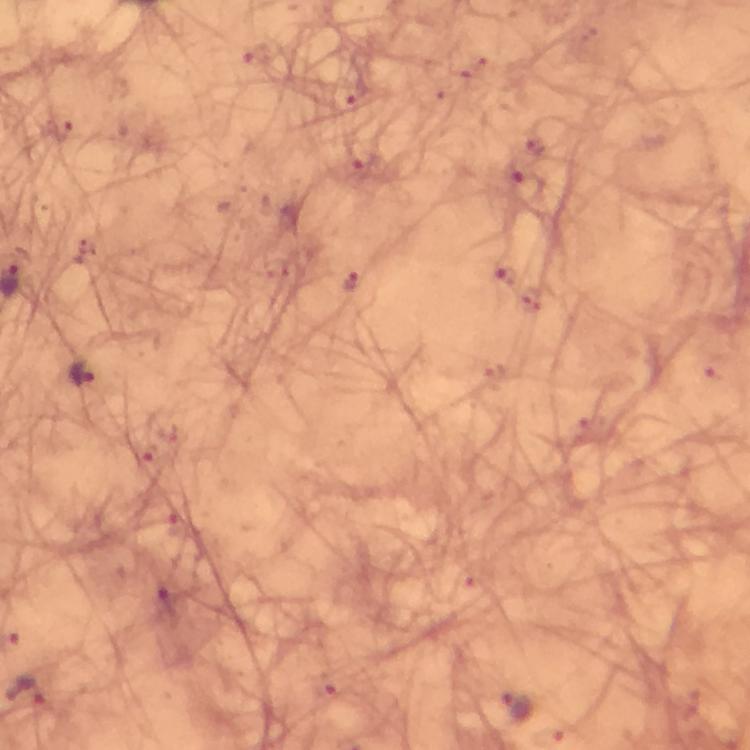 Approximate object centers, in pixels from the top-left corner. Plasmodium parasite locations: (x=350, y=283), (x=83, y=374), (x=27, y=695), (x=514, y=708). Cropped region of a single field of view. From a diagnostic examination for malaria. 100x magnification. Image is 750×750 pixels. Immersion oil was used. Giemsa-stained preparation. Thick blood smear. Photographed with a smartphone mounted on the microscope.